Assess for Plasmodium parasites.
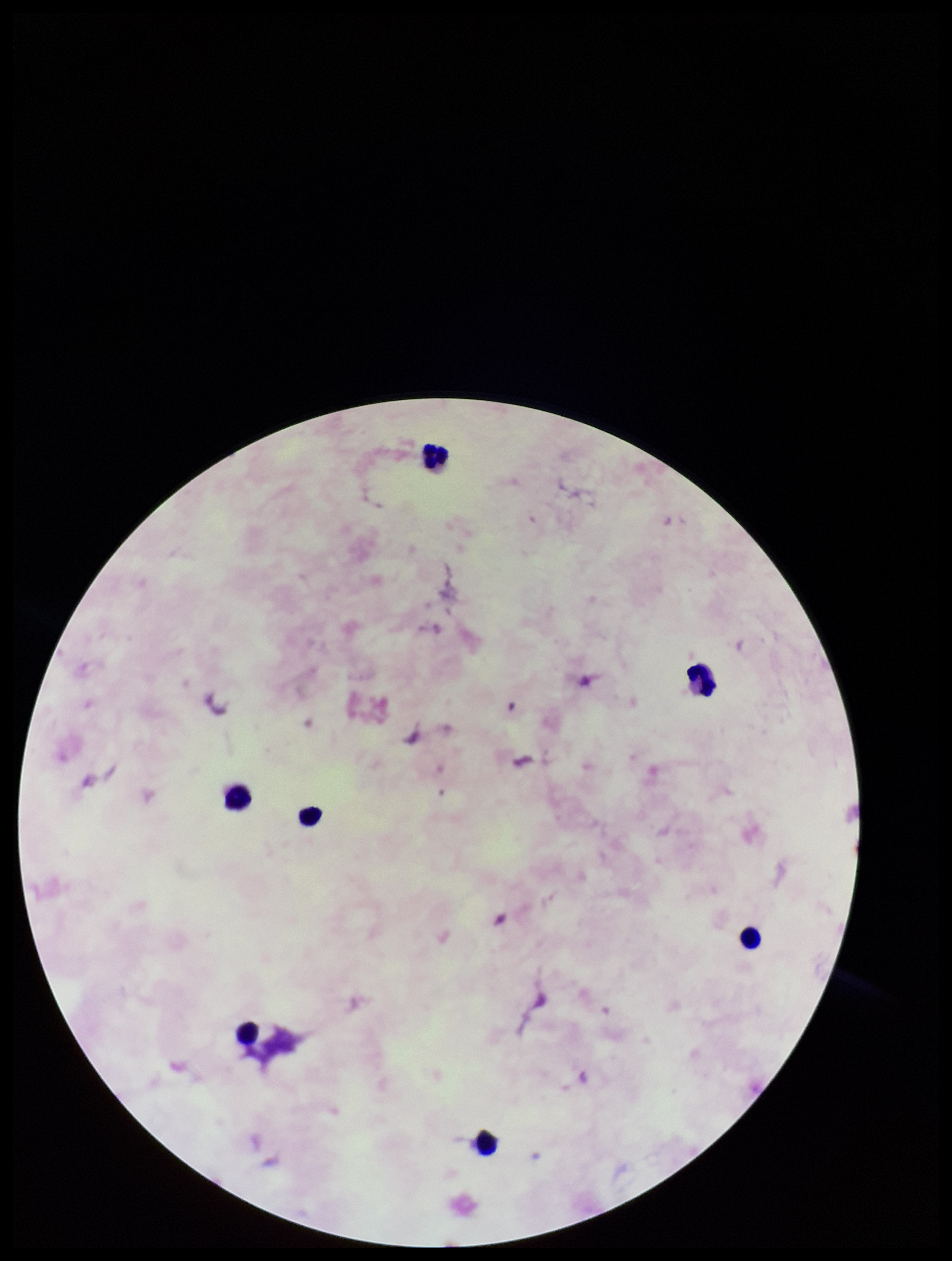
None detected.

patient_malaria_status: negative
preparation: thick blood smear
leukocyte_count: 7
parasite_count: 0
field_of_view: single
capture: smartphone photograph through the microscope eyepiece
stain: Giemsa
image_size: 952×1261 pixels